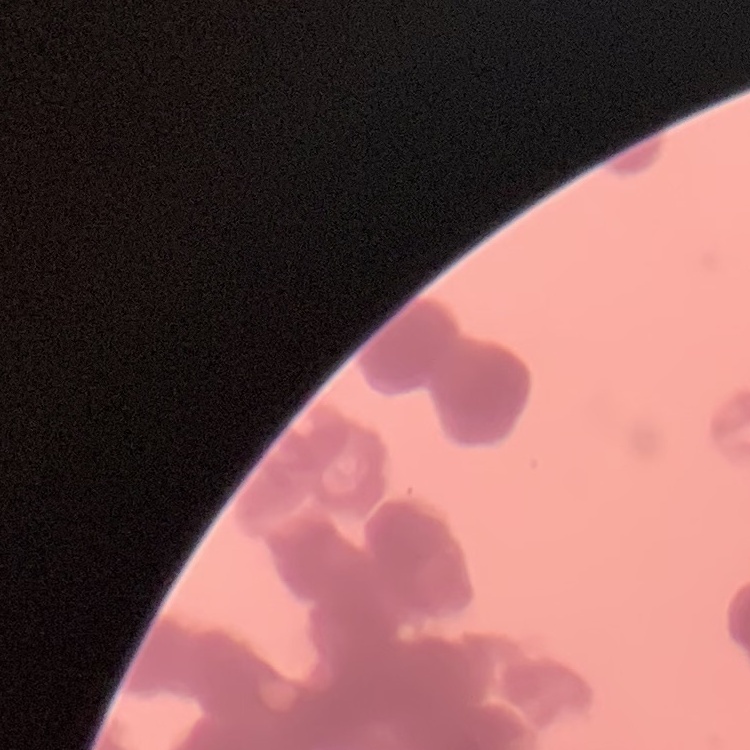
Summary:
  - Red blood cell morphology: rouleaux formation
  - Stain: Field's or Giemsa
  - Preparation: thin blood film
  - Image type: square crop of a larger photomicrograph